Report the malaria status of this cell.
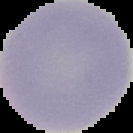

It is uninfected.

image type = segmented cell region with the area outside set to black
image size = 133×133 pixels
preparation = thin blood film